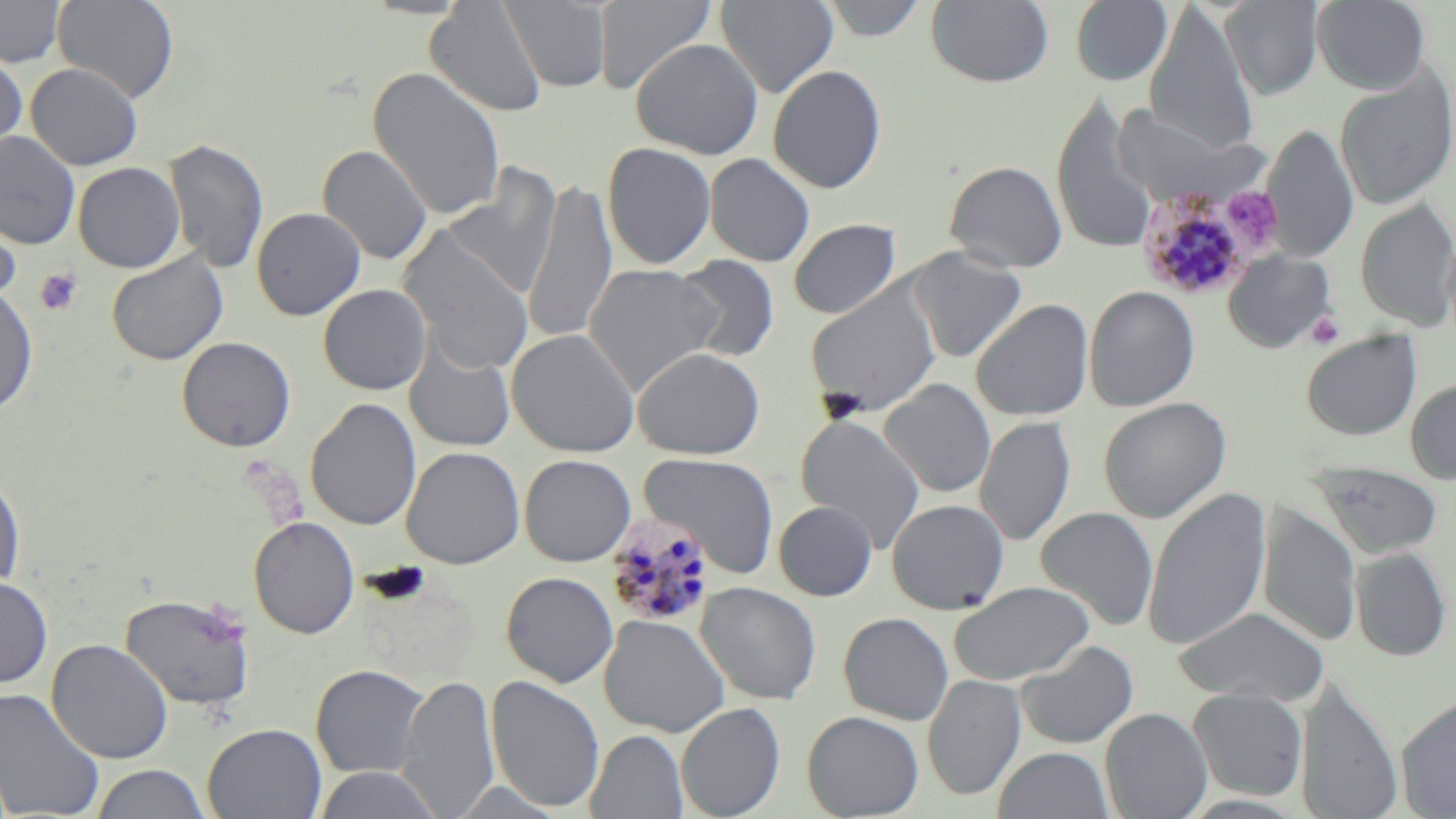

slide-level diagnosis = Plasmodium malariae
image size = 1456×819 pixels
preparation = thin blood smear
uninfected red blood cell locations = approximate bounding boxes as (x1, y1, x2, y2) in pixels: (0, 0, 66, 67), (53, 0, 179, 103), (425, 0, 548, 118), (594, 0, 717, 94), (716, 0, 839, 97), (817, 0, 930, 41), (1071, 0, 1173, 86), (1312, 0, 1431, 93), (501, 1, 612, 92), (926, 1, 1054, 88), (1220, 1, 1325, 99), (1144, 3, 1259, 155), (631, 38, 763, 159), (0, 50, 28, 158), (25, 63, 143, 170), (768, 64, 887, 194), (368, 66, 506, 221), (1335, 67, 1456, 210), (1052, 96, 1159, 254), (1111, 106, 1248, 207), (1263, 124, 1358, 264), (0, 130, 80, 249), (164, 138, 269, 275), (603, 141, 717, 269), (317, 144, 433, 265), (705, 153, 815, 266), (944, 160, 1068, 272), (73, 162, 186, 273), (442, 166, 561, 300), (524, 178, 617, 346), (1355, 197, 1456, 331), (0, 199, 22, 306), (251, 207, 366, 320), (788, 219, 900, 319), (397, 227, 534, 375), (905, 247, 1028, 363), (1223, 249, 1337, 353), (106, 252, 228, 365), (673, 255, 780, 363), (584, 263, 722, 397), (804, 282, 942, 417), (318, 284, 431, 394), (0, 286, 38, 417), (1084, 286, 1200, 411), (971, 299, 1094, 421), (506, 328, 640, 457), (1301, 329, 1422, 441), (176, 336, 296, 452), (404, 338, 516, 453), (633, 347, 765, 459), (1405, 377, 1456, 485), (879, 378, 996, 498), (305, 397, 422, 531), (1099, 397, 1231, 523), (796, 413, 926, 553), (976, 416, 1076, 547), (401, 445, 525, 569), (639, 452, 780, 576), (519, 454, 636, 566), (1308, 462, 1445, 560), (0, 469, 25, 594), (1143, 487, 1271, 651), (886, 499, 1010, 615), (774, 501, 877, 601), (1258, 504, 1361, 647), (1036, 506, 1159, 631), (248, 516, 360, 639), (1351, 547, 1452, 661), (501, 572, 619, 688), (0, 575, 53, 689), (949, 581, 1095, 685), (696, 582, 821, 705), (119, 592, 257, 712), (1172, 606, 1330, 705), (838, 612, 954, 725), (599, 614, 730, 738), (46, 639, 173, 764), (1018, 640, 1139, 750), (311, 664, 430, 778), (923, 673, 1026, 801), (397, 674, 499, 817), (485, 675, 605, 813), (0, 686, 105, 818), (1297, 687, 1402, 819), (1188, 688, 1309, 800), (1396, 693, 1456, 817), (676, 701, 786, 818), (1100, 707, 1212, 819), (801, 710, 924, 818), (203, 722, 326, 819), (586, 729, 688, 818), (993, 746, 1115, 819), (90, 764, 213, 819), (313, 766, 445, 819)
modality = optical microscopy
stain = May-Grünwald-Giemsa
Plasmodium malariae-infected red blood cell locations = approximate bounding boxes as (x1, y1, x2, y2) in pixels: (1137, 185, 1256, 301), (604, 513, 716, 629)
magnification = 1000x
field of view = single
platelet locations = approximate bounding boxes as (x1, y1, x2, y2) in pixels: (1223, 186, 1283, 250), (36, 269, 82, 315), (1306, 310, 1345, 349)